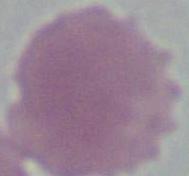
Micrograph. A red blood cell is shown. Captured at 1000x magnification.